State which parasite is depicted.
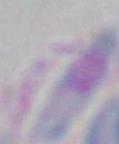
Toxoplasma gondii.

magnification = 1000x
modality = micrograph